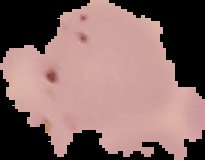

Summary:
  - Image type: segmented cell region on a black background
  - Result: Plasmodium parasites detected
  - Preparation: thin blood film
  - Image size: 205×160 pixels